Report the malaria status of this cell.
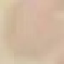
It is uninfected.

capture: smartphone through the microscope eyepiece
preparation: thin blood smear
stain: Giemsa
image_type: automatically extracted cell patch, resized to 64 × 64 pixels